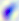 Photomicrograph. Captured at 400x magnification. Toxoplasma gondii is seen.